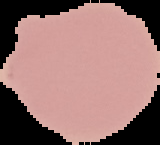 Image is 160×145 pixels. Segmented cell region on a black background. Result: no Plasmodium parasites detected. From a thin blood smear.